Classify this cell by malaria status.
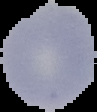
It is uninfected.

image size = 97×112 pixels
preparation = thin blood smear
image type = cell region segmented out of the field of view; surrounding area masked to black